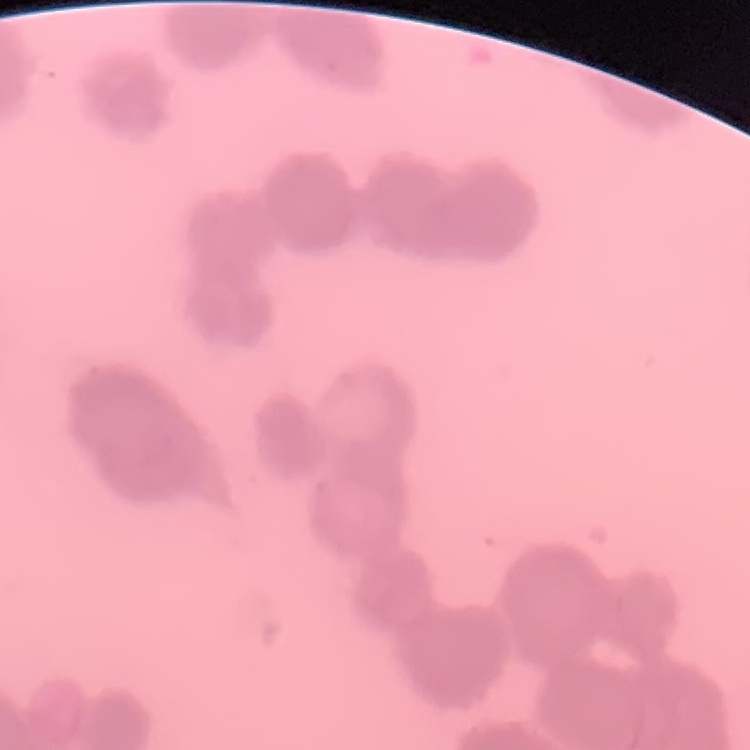

erythrocyte morphology = rouleaux formation
preparation = thin blood smear
stain = Field's or Giemsa
image type = square crop of a larger photomicrograph